Report the malaria status of this cell.
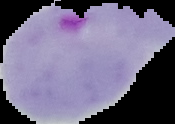

It is parasitized.

Segmented cell region on a black background. Image is 175×124 pixels. From a thin blood film.